Name the parasite shown.
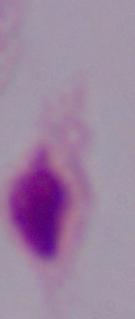
A trichomonad.

modality = micrograph
magnification = 1000x